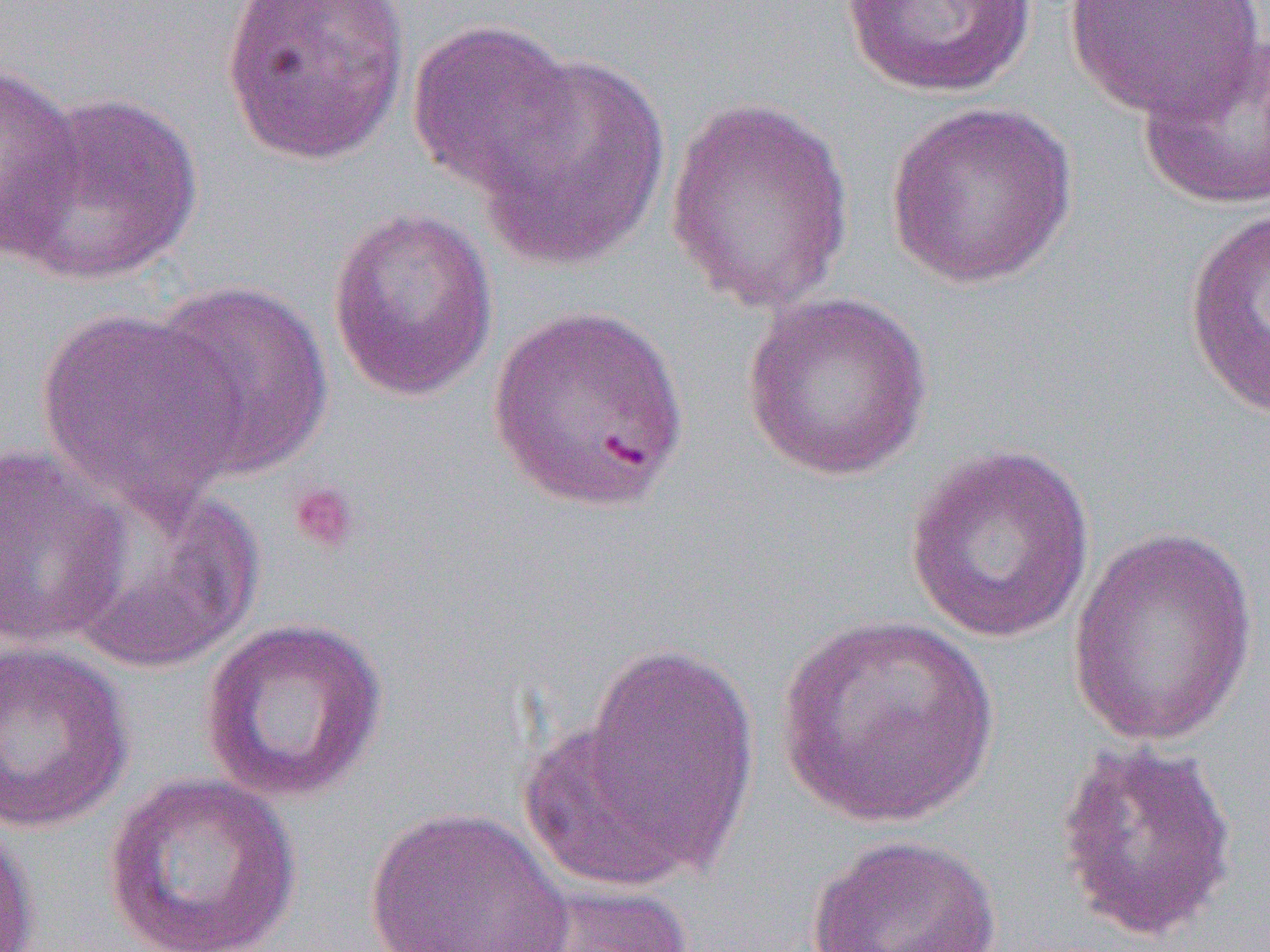

Summary:
  - Coordinate format: approximate bounding boxes as named x1/y1/x2/y2 corners in pixels
  - Platelet locations: (x1=286, y1=480, x2=362, y2=556)
  - Uninfected red blood cell locations: (x1=215, y1=0, x2=411, y2=167), (x1=840, y1=0, x2=1038, y2=99), (x1=1063, y1=0, x2=1266, y2=120), (x1=407, y1=20, x2=580, y2=198), (x1=1136, y1=36, x2=1269, y2=212), (x1=475, y1=51, x2=673, y2=270), (x1=0, y1=62, x2=85, y2=258), (x1=7, y1=90, x2=204, y2=287), (x1=664, y1=97, x2=856, y2=314), (x1=883, y1=101, x2=1079, y2=291), (x1=326, y1=206, x2=498, y2=402), (x1=1183, y1=206, x2=1270, y2=421), (x1=145, y1=280, x2=333, y2=479), (x1=741, y1=291, x2=934, y2=482), (x1=486, y1=304, x2=690, y2=514), (x1=35, y1=307, x2=244, y2=515), (x1=0, y1=442, x2=135, y2=652), (x1=903, y1=443, x2=1097, y2=644), (x1=57, y1=475, x2=264, y2=673), (x1=1066, y1=522, x2=1260, y2=752), (x1=774, y1=614, x2=999, y2=829), (x1=197, y1=616, x2=390, y2=804), (x1=558, y1=637, x2=761, y2=889), (x1=0, y1=641, x2=137, y2=833), (x1=1053, y1=737, x2=1240, y2=945), (x1=103, y1=772, x2=301, y2=951), (x1=363, y1=806, x2=574, y2=952), (x1=0, y1=816, x2=40, y2=952), (x1=805, y1=833, x2=1004, y2=952), (x1=505, y1=882, x2=696, y2=952)
  - Slide-level diagnosis: Plasmodium falciparum
  - Magnification: 1000x
  - Preparation: thin blood film
  - Field of view: single
  - Modality: light microscopy
  - Image size: 1270×952 pixels